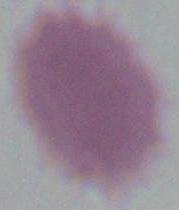
Summary:
  - Magnification: 1000x
  - Identification: erythrocyte
  - Modality: photomicrograph